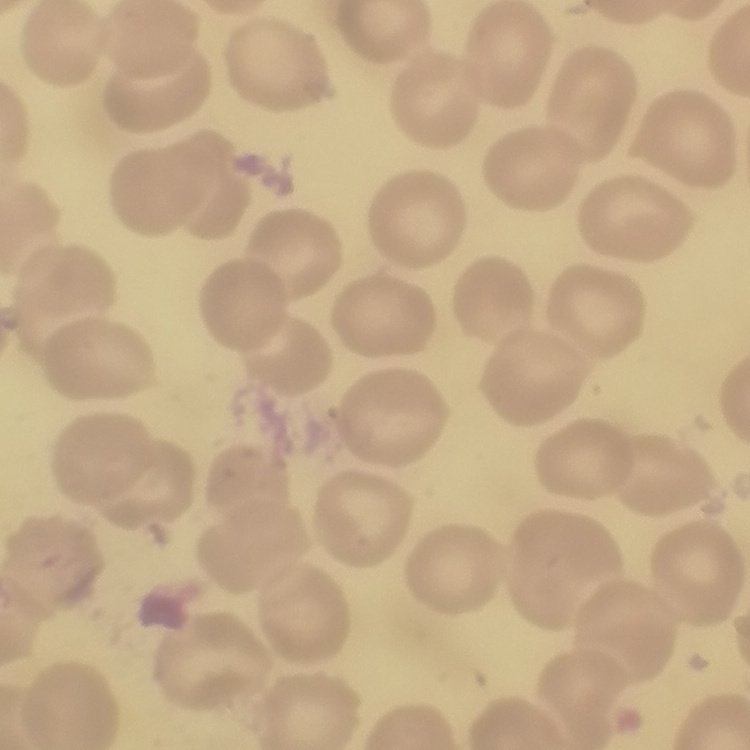
erythrocyte morphology = no rouleaux formation
stain = Field's or Giemsa
image type = square crop of a larger photomicrograph
preparation = thin blood film